Classify this cell by malaria status.
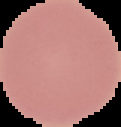
It is uninfected.

{
  "image_type": "segmented cell region on a black background",
  "preparation": "thin blood film",
  "image_size": "121×127 pixels"
}